Assess the morphology of the erythrocytes.
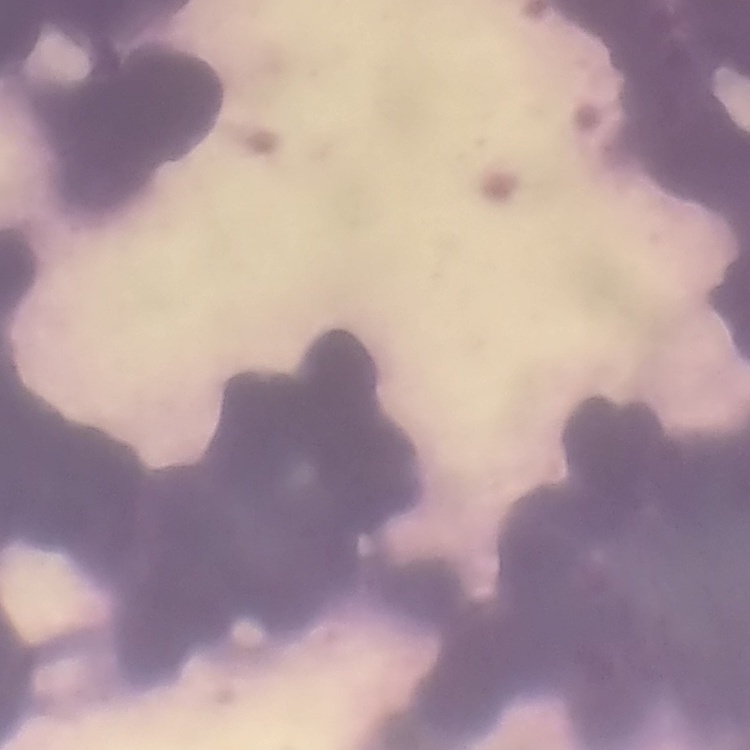

They show rouleaux formation.

Summary:
  - Preparation: thin peripheral smear
  - Stain: Field's or Giemsa
  - Image type: one tile cut from a larger photomicrograph